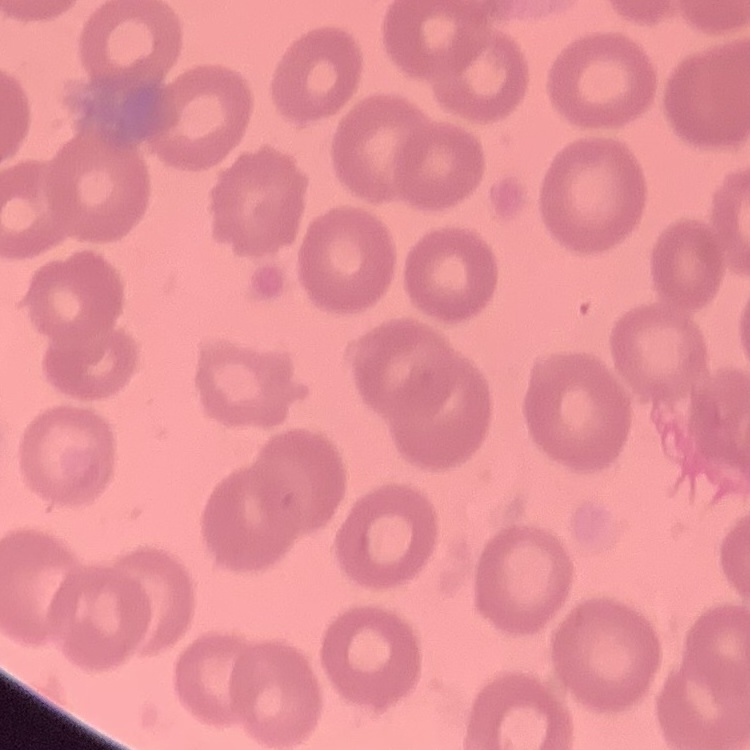
Summary:
  - Red blood cell morphology: no rouleaux formation
  - Preparation: thin blood film
  - Image type: square crop of a larger photomicrograph
  - Stain: Field's or Giemsa